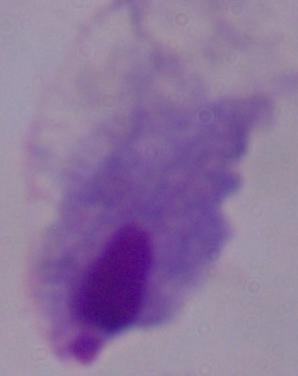

Summary:
  - Identification: trichomonad
  - Modality: photomicrograph
  - Magnification: 1000x